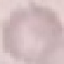

Summary:
  - Malaria status: uninfected
  - Image type: cell patch, automatically extracted from a larger field of view and resized to 64 × 64 pixels
  - Stain: Giemsa
  - Capture: smartphone through the microscope eyepiece
  - Preparation: thin blood film